State the blood parasite species.
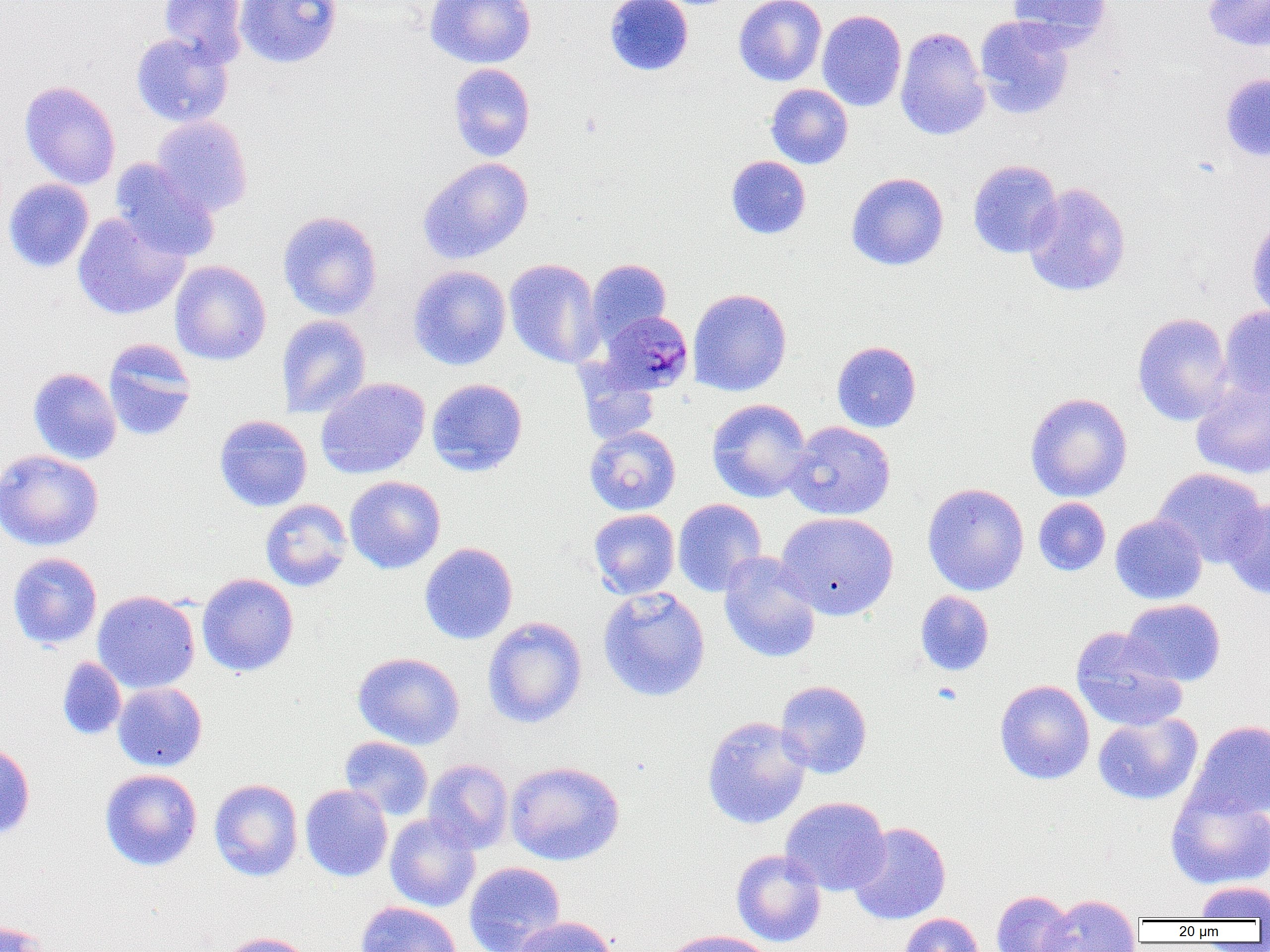

Plasmodium malariae.

modality = light microscopy
Plasmodium malariae-infected red blood cell locations = approximate bounding boxes as (x1,y1)-(x2,y2) corner pairs in pixels: (597,311)-(693,394)
preparation = thin blood smear
image size = 1270×952 pixels
uninfected red blood cell locations = approximate bounding boxes as (x1,y1)-(x2,y2) corner pairs in pixels: (159,0)-(248,66), (235,0)-(342,68), (424,0)-(537,69), (604,0)-(693,76), (733,0)-(826,87), (1007,0)-(1112,49), (1203,0)-(1270,52), (817,10)-(907,111), (973,16)-(1075,120), (894,27)-(991,141), (130,32)-(233,127), (447,63)-(535,162), (1219,72)-(1270,162), (19,81)-(121,190), (765,83)-(853,169), (151,116)-(253,216), (726,155)-(811,239), (418,157)-(534,264), (110,158)-(220,261), (967,159)-(1064,259), (846,172)-(949,271), (2,178)-(94,273), (1022,183)-(1131,297), (277,210)-(383,320), (72,212)-(189,320), (1246,219)-(1270,321), (504,258)-(604,368), (586,259)-(671,345), (169,260)-(271,365), (408,265)-(512,371), (687,288)-(792,396), (1219,306)-(1270,401), (1132,312)-(1234,426), (276,314)-(372,418), (103,339)-(198,441), (831,341)-(922,432), (27,367)-(122,465), (577,370)-(661,445), (315,377)-(430,479), (426,378)-(528,476), (1191,381)-(1270,480), (1025,392)-(1133,502), (707,398)-(812,503), (213,414)-(313,512), (785,421)-(896,521), (584,425)-(681,515), (0,449)-(104,551), (1152,468)-(1267,567), (344,475)-(446,573), (922,483)-(1029,596), (1033,497)-(1111,576), (1221,497)-(1270,600), (260,498)-(353,592), (672,499)-(767,596), (588,509)-(680,599), (775,511)-(899,620), (1110,514)-(1207,605), (419,542)-(518,644), (718,551)-(822,664), (8,552)-(102,650), (196,572)-(299,677), (597,587)-(711,702), (92,590)-(200,694), (915,591)-(994,676), (1121,599)-(1226,687), (482,616)-(587,728), (1070,627)-(1187,732), (353,652)-(465,750), (57,657)-(127,740), (775,680)-(873,778), (994,680)-(1095,784), (112,682)-(207,772), (1092,713)-(1202,805), (702,716)-(811,830), (1186,719)-(1270,821), (339,736)-(434,820), (0,740)-(35,842), (423,758)-(514,854), (505,760)-(625,866), (99,768)-(203,871), (209,778)-(303,881), (300,784)-(392,882), (1165,788)-(1270,890), (780,796)-(891,896), (384,813)-(481,912), (848,822)-(951,925), (731,849)-(826,947), (464,861)-(566,952), (1195,881)-(1270,920), (990,890)-(1076,952), (1041,894)-(1142,952), (356,901)-(462,952), (897,913)-(984,952), (512,916)-(618,952), (0,919)-(56,951), (659,930)-(777,952), (216,932)-(318,952)
field of view = single
magnification = 1000x